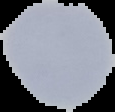

Summary:
  - Preparation: thin blood smear
  - Result: negative for malaria parasites
  - Image size: 115×112 pixels
  - Image type: segmented cell region with the area outside set to black